Give the position of every Plasmodium parasite.
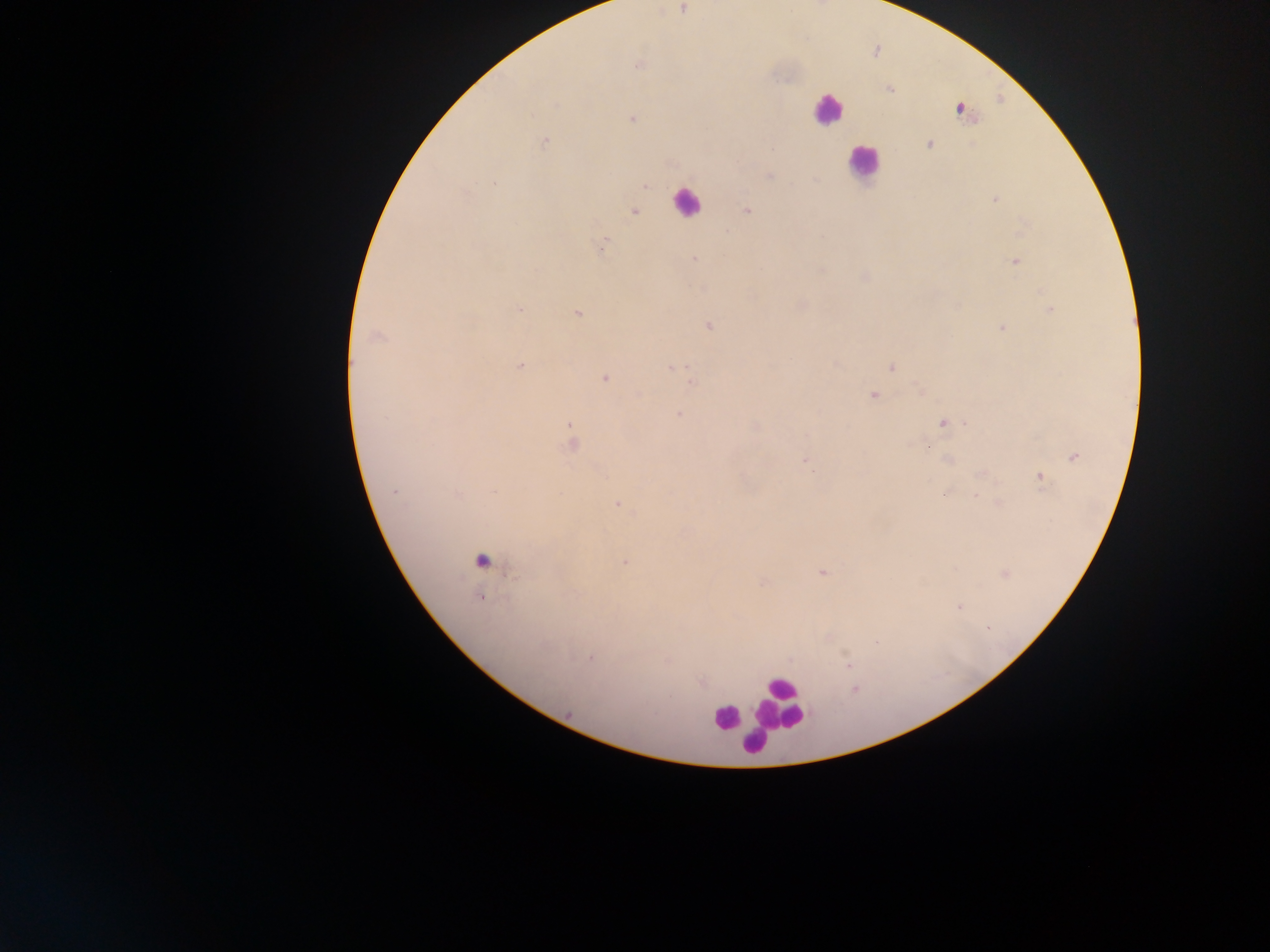

Approximate centers as [x, y] in pixels.
Plasmodium parasites: [682, 9], [638, 66], [889, 88], [959, 109], [632, 119], [543, 141], [930, 144], [769, 175], [496, 185], [644, 185], [995, 200], [746, 210], [634, 211], [602, 246], [694, 259], [1015, 261], [864, 276], [1051, 309], [520, 310], [577, 312], [709, 325], [1003, 328], [376, 336], [520, 365], [891, 367], [672, 368], [605, 377], [692, 383], [923, 392], [874, 394], [679, 414], [943, 422], [966, 423], [570, 426], [756, 426], [571, 439], [928, 447], [1073, 456], [806, 459], [983, 473], [1039, 476], [944, 493], [976, 496], [999, 502], [616, 503], [481, 559], [625, 562], [821, 572], [1005, 574], [762, 581], [480, 596], [958, 606], [590, 658], [847, 661], [854, 689].

Leukocyte locations: [827, 108], [862, 162], [688, 202], [779, 701], [742, 715], [727, 717], [754, 743]. Mobile-phone photograph taken through the microscope. Image is 1270×952 pixels. Sample from Ghana. One field of view. Thick blood film.